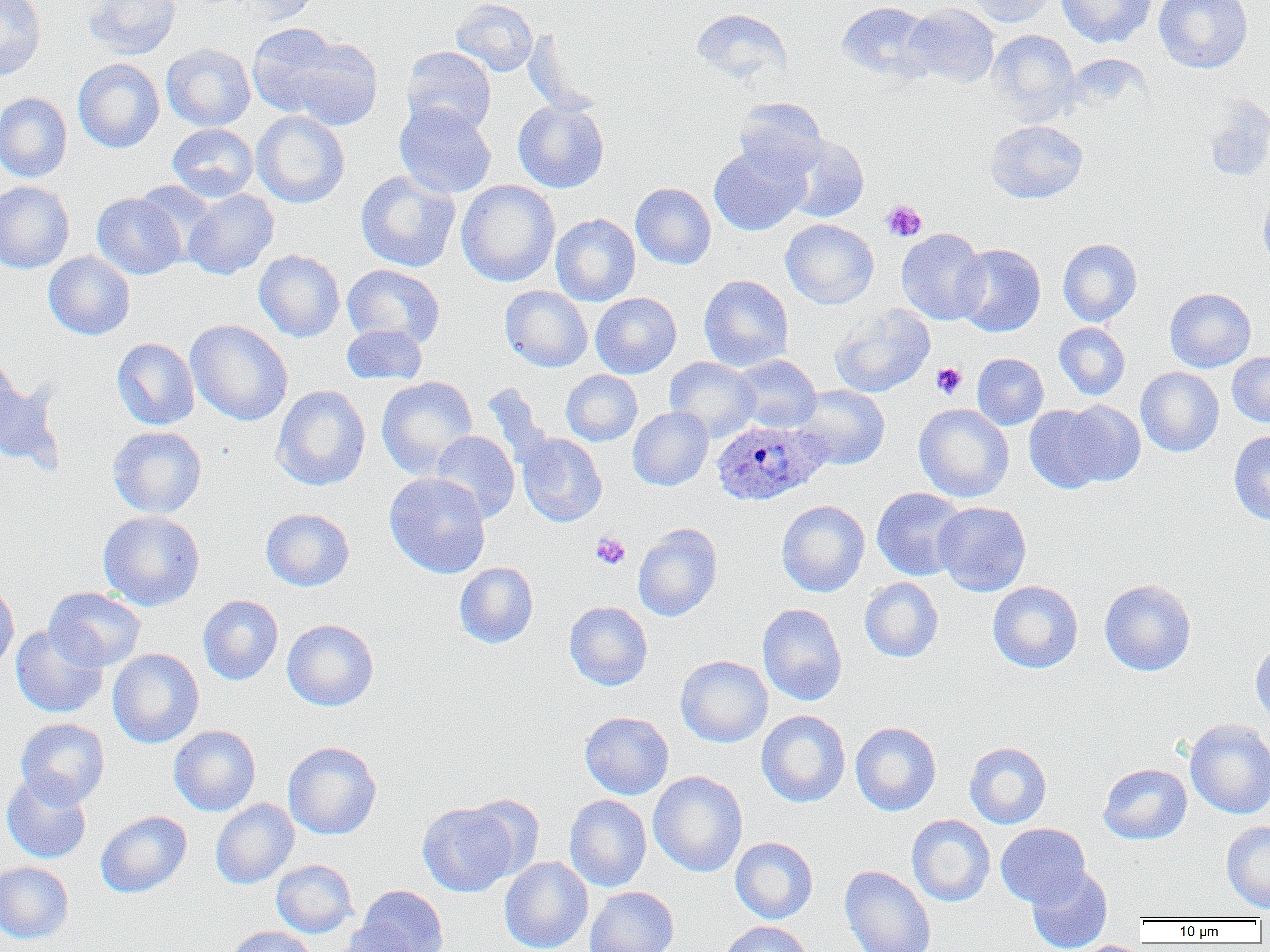

slide-level diagnosis = Plasmodium ovale
modality = light microscopy
magnification = 1000x
preparation = thin blood film
field of view = one of a larger specimen
Plasmodium ovale-infected red blood cell locations = approximate bounding boxes as (x1, y1, x2, y2) in pixels: (710, 419, 828, 506)
uninfected red blood cell locations = approximate bounding boxes as (x1, y1, x2, y2) in pixels: (0, 0, 46, 80), (82, 0, 181, 59), (236, 0, 322, 24), (451, 0, 538, 77), (963, 0, 1056, 27), (1057, 0, 1157, 48), (1154, 0, 1252, 74), (836, 1, 937, 84), (902, 2, 999, 88), (690, 9, 794, 86), (247, 22, 352, 119), (986, 29, 1079, 122), (287, 37, 383, 132), (161, 43, 255, 132), (401, 46, 496, 136), (73, 58, 165, 153), (0, 92, 72, 182), (733, 97, 827, 178), (1203, 97, 1270, 181), (513, 99, 610, 193), (394, 103, 496, 199), (252, 110, 350, 208), (985, 120, 1088, 204), (167, 123, 258, 202), (780, 134, 869, 222), (709, 144, 809, 236), (355, 170, 461, 272), (456, 180, 560, 287), (0, 181, 75, 273), (135, 182, 220, 263), (631, 183, 716, 269), (1258, 186, 1270, 269), (183, 189, 279, 279), (92, 193, 186, 279), (551, 214, 640, 306), (780, 218, 879, 309), (896, 228, 988, 325), (1057, 239, 1142, 326), (953, 244, 1046, 337), (254, 250, 345, 342), (43, 251, 135, 340), (342, 264, 445, 348), (699, 275, 793, 371), (500, 285, 593, 372), (1164, 287, 1255, 372), (590, 293, 681, 378), (829, 304, 935, 397), (185, 320, 293, 426), (1054, 322, 1130, 400), (342, 323, 427, 385), (111, 338, 200, 430), (0, 352, 23, 437), (1227, 352, 1270, 426), (972, 353, 1048, 430), (731, 354, 822, 433), (665, 357, 760, 442), (1135, 367, 1224, 456), (561, 370, 643, 446), (377, 376, 478, 478), (0, 377, 63, 471), (481, 383, 552, 467), (271, 385, 370, 491), (793, 385, 890, 470), (1059, 400, 1146, 488), (914, 403, 1014, 502), (1024, 403, 1114, 493), (627, 407, 714, 491), (107, 426, 207, 518), (1228, 430, 1270, 526), (429, 431, 520, 523), (517, 433, 607, 526), (384, 472, 490, 578), (871, 488, 969, 581), (776, 500, 870, 597), (933, 502, 1032, 596), (261, 508, 354, 591), (98, 510, 205, 611), (633, 523, 723, 622), (454, 562, 538, 648), (859, 577, 943, 662), (1099, 578, 1196, 676), (0, 580, 19, 673), (987, 580, 1083, 673), (44, 587, 146, 672), (198, 595, 283, 685), (564, 601, 653, 690), (757, 603, 847, 705), (282, 619, 378, 710), (11, 624, 108, 718), (1250, 639, 1270, 728), (107, 649, 204, 748), (675, 655, 773, 747), (756, 710, 851, 807), (580, 712, 674, 799), (15, 717, 110, 808), (1184, 718, 1270, 819), (850, 722, 941, 816), (169, 725, 261, 816), (283, 741, 381, 840), (964, 742, 1052, 829), (1098, 763, 1192, 845), (648, 771, 748, 877), (1, 772, 92, 864), (465, 795, 544, 879), (564, 795, 651, 891), (210, 798, 299, 889), (418, 802, 520, 896), (95, 810, 192, 898), (907, 814, 995, 907), (1221, 820, 1270, 912), (995, 823, 1091, 908), (730, 837, 818, 924), (499, 857, 593, 952), (271, 859, 357, 938), (0, 861, 74, 943), (839, 865, 936, 952), (1026, 865, 1113, 952), (355, 885, 448, 952), (584, 886, 679, 952), (337, 920, 420, 952), (717, 920, 815, 952), (225, 926, 317, 952), (1068, 939, 1153, 952)
platelet locations = approximate bounding boxes as (x1, y1, x2, y2) in pixels: (881, 200, 927, 241), (931, 362, 967, 399), (591, 532, 630, 569)
image size = 1270×952 pixels